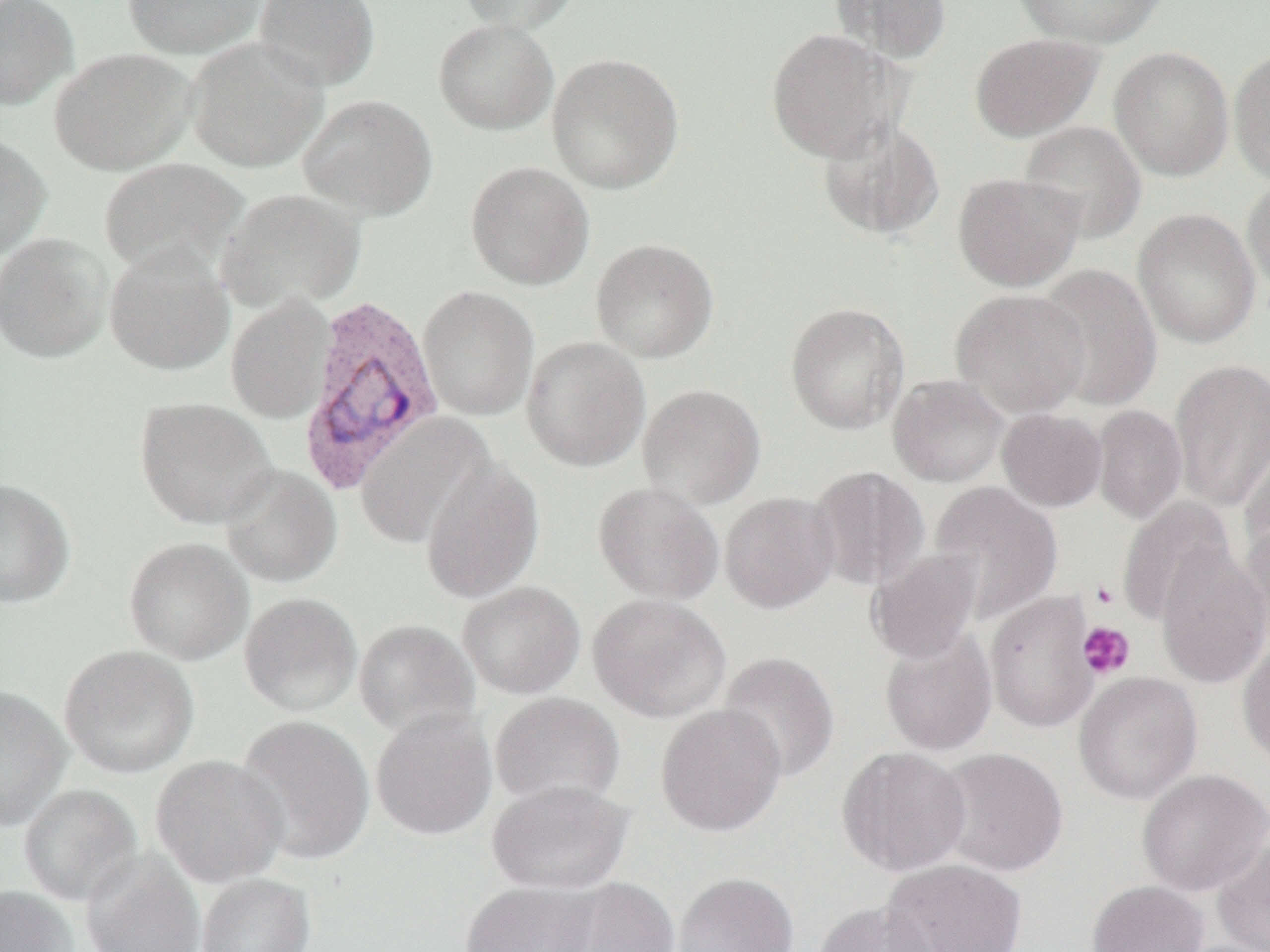

Summary:
  - Coordinate format: approximate bounding boxes as named x1/y1/x2/y2 corners in pixels
  - Uninfected red blood cell locations: (x1=0, y1=0, x2=78, y2=110), (x1=121, y1=0, x2=269, y2=59), (x1=254, y1=0, x2=380, y2=91), (x1=456, y1=0, x2=579, y2=34), (x1=831, y1=0, x2=952, y2=64), (x1=1012, y1=0, x2=1168, y2=48), (x1=433, y1=18, x2=559, y2=135), (x1=764, y1=27, x2=901, y2=161), (x1=969, y1=32, x2=1104, y2=141), (x1=185, y1=36, x2=329, y2=173), (x1=1108, y1=46, x2=1234, y2=181), (x1=50, y1=48, x2=197, y2=175), (x1=1229, y1=48, x2=1270, y2=186), (x1=546, y1=52, x2=684, y2=194), (x1=298, y1=94, x2=438, y2=221), (x1=818, y1=117, x2=946, y2=241), (x1=1019, y1=120, x2=1147, y2=242), (x1=0, y1=132, x2=51, y2=260), (x1=98, y1=157, x2=248, y2=278), (x1=465, y1=161, x2=595, y2=289), (x1=953, y1=172, x2=1084, y2=291), (x1=1242, y1=174, x2=1270, y2=297), (x1=216, y1=188, x2=366, y2=314), (x1=1132, y1=207, x2=1261, y2=349), (x1=0, y1=233, x2=112, y2=364), (x1=590, y1=238, x2=719, y2=363), (x1=104, y1=244, x2=235, y2=376), (x1=1036, y1=263, x2=1162, y2=410), (x1=418, y1=285, x2=539, y2=421), (x1=951, y1=288, x2=1091, y2=418), (x1=226, y1=295, x2=334, y2=424), (x1=785, y1=301, x2=910, y2=434), (x1=521, y1=336, x2=651, y2=471), (x1=1169, y1=359, x2=1270, y2=511), (x1=888, y1=374, x2=1009, y2=487), (x1=637, y1=383, x2=766, y2=510), (x1=134, y1=398, x2=277, y2=529), (x1=1092, y1=405, x2=1187, y2=524), (x1=997, y1=408, x2=1107, y2=512), (x1=353, y1=412, x2=497, y2=550), (x1=1239, y1=431, x2=1270, y2=561), (x1=420, y1=459, x2=545, y2=603), (x1=219, y1=463, x2=343, y2=588), (x1=808, y1=466, x2=929, y2=593), (x1=0, y1=478, x2=76, y2=608), (x1=928, y1=481, x2=1063, y2=622), (x1=593, y1=482, x2=724, y2=604), (x1=720, y1=491, x2=840, y2=613), (x1=1115, y1=497, x2=1235, y2=627), (x1=1239, y1=516, x2=1270, y2=649), (x1=123, y1=536, x2=253, y2=665), (x1=1155, y1=544, x2=1269, y2=688), (x1=868, y1=548, x2=983, y2=664), (x1=457, y1=581, x2=586, y2=699), (x1=985, y1=591, x2=1099, y2=733), (x1=239, y1=592, x2=362, y2=717), (x1=588, y1=593, x2=732, y2=723), (x1=353, y1=618, x2=481, y2=740), (x1=880, y1=627, x2=998, y2=756), (x1=1237, y1=640, x2=1270, y2=768), (x1=58, y1=644, x2=200, y2=778), (x1=718, y1=651, x2=840, y2=782), (x1=1073, y1=671, x2=1203, y2=805), (x1=0, y1=685, x2=72, y2=830), (x1=490, y1=691, x2=625, y2=811), (x1=655, y1=703, x2=788, y2=836), (x1=370, y1=709, x2=497, y2=841), (x1=234, y1=714, x2=376, y2=865), (x1=837, y1=746, x2=972, y2=876), (x1=936, y1=747, x2=1068, y2=877), (x1=150, y1=754, x2=288, y2=887), (x1=1137, y1=768, x2=1270, y2=895), (x1=486, y1=779, x2=634, y2=895), (x1=18, y1=783, x2=142, y2=906), (x1=1211, y1=837, x2=1270, y2=952), (x1=81, y1=851, x2=205, y2=952), (x1=882, y1=859, x2=1027, y2=952), (x1=672, y1=872, x2=799, y2=952), (x1=196, y1=873, x2=316, y2=952), (x1=552, y1=877, x2=680, y2=952), (x1=459, y1=880, x2=601, y2=952), (x1=1087, y1=880, x2=1209, y2=952), (x1=0, y1=886, x2=78, y2=952), (x1=812, y1=900, x2=936, y2=952)
  - Platelet locations: (x1=1090, y1=579, x2=1120, y2=610), (x1=1077, y1=621, x2=1135, y2=679)
  - Plasmodium vivax-infected red blood cell locations: (x1=298, y1=293, x2=447, y2=496)
  - Slide-level diagnosis: Plasmodium vivax
  - Field of view: one of a larger specimen
  - Modality: light microscopy
  - Magnification: 1000x
  - Preparation: thin blood film
  - Image size: 1270×952 pixels